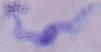
A trypanosome is shown. Photomicrograph. Captured at 1000x magnification.